Name the parasite shown.
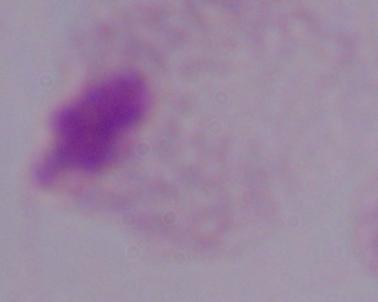

A trichomonad.

Summary:
  - Magnification: 1000x
  - Modality: micrograph